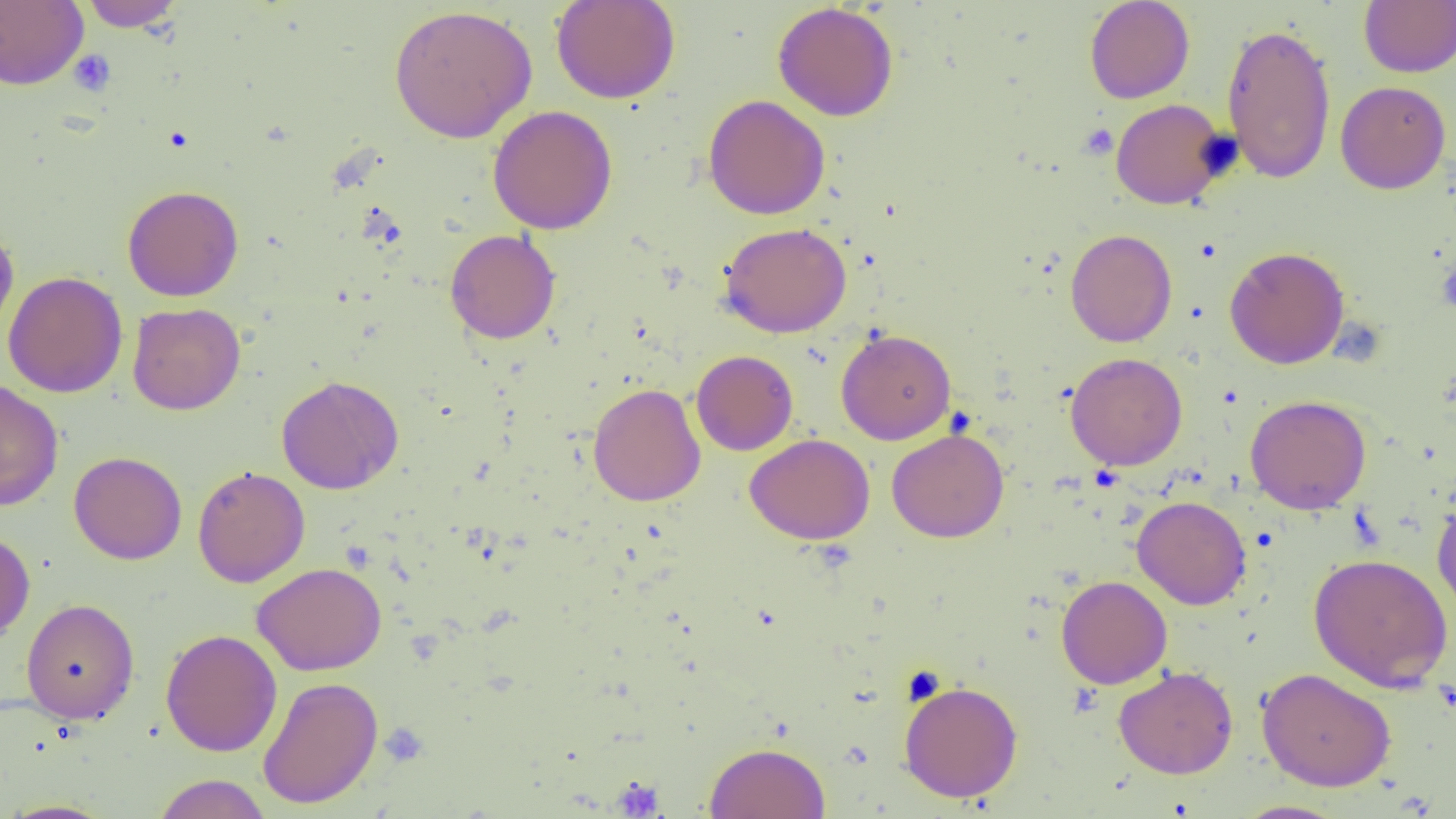
slide_level_diagnosis: no evidence of blood parasites
preparation: thin blood smear
magnification: 1000x
modality: optical microscopy
image_size: 1456×819 pixels
platelet_locations: 'approximate bounding boxes as (x1, y1, x2, y2) in pixels: (68, 49, 116, 97), (1078, 124, 1120, 161), (1436, 259, 1456, 316), (381, 723, 429, 768), (612, 777, 665, 817)'
field_of_view: one of a larger specimen
uninfected_red_blood_cell_locations: 'approximate bounding boxes as (x1, y1, x2, y2) in pixels: (78, 0, 186, 31), (551, 0, 680, 104), (1084, 0, 1195, 104), (1359, 0, 1456, 78), (0, 1, 89, 89), (772, 3, 899, 122), (388, 4, 538, 144), (1221, 23, 1337, 183), (1335, 80, 1451, 193), (703, 94, 830, 219), (1110, 99, 1230, 209), (488, 105, 618, 234), (122, 185, 244, 302), (718, 221, 852, 338), (0, 226, 19, 344), (445, 229, 561, 344), (1065, 229, 1177, 348), (1224, 246, 1350, 369), (3, 271, 128, 397), (127, 302, 245, 415), (835, 328, 956, 444), (691, 350, 798, 456), (1065, 352, 1187, 470), (276, 375, 404, 495), (0, 378, 64, 511), (588, 383, 705, 506), (1245, 394, 1372, 514), (886, 428, 1009, 543), (745, 434, 875, 544), (68, 450, 187, 565), (192, 465, 310, 587), (1132, 495, 1251, 610), (1432, 495, 1456, 624), (0, 529, 35, 644), (1308, 552, 1453, 692), (252, 562, 387, 676), (1056, 575, 1172, 689), (21, 598, 140, 724), (160, 629, 282, 756), (1113, 665, 1238, 779), (1257, 667, 1396, 791), (257, 676, 383, 808), (898, 679, 1023, 802), (704, 742, 830, 819), (152, 774, 272, 819), (0, 800, 118, 818), (1234, 800, 1349, 818)'